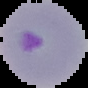 Result: malaria parasites identified. Segmented cell region on a black background. Image is 88×88 pixels. From a thin blood film.